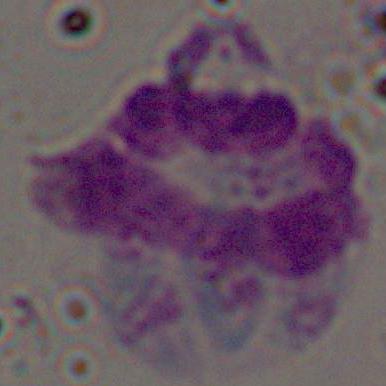

modality = photomicrograph
magnification = 1000x
identification = white blood cell